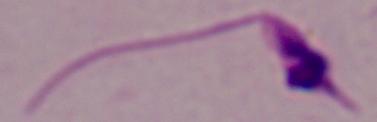

{
  "magnification": "1000x",
  "modality": "micrograph",
  "identification": "Leishmania"
}